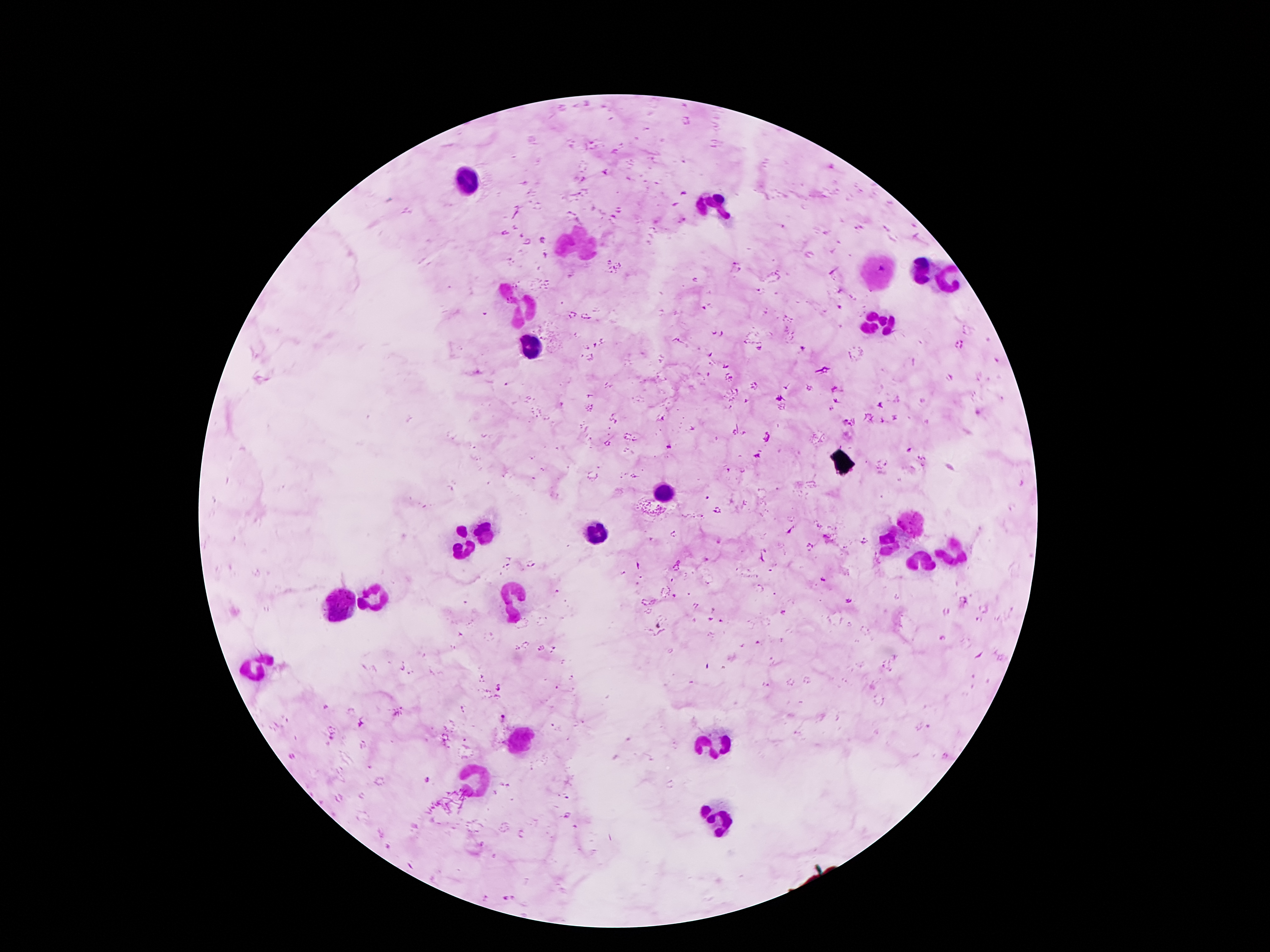

Approximate object centers, in pixels from the top-left corner.
Summary:
  - Plasmodium parasite locations: (x=736, y=260), (x=845, y=421), (x=850, y=425), (x=669, y=447), (x=707, y=497), (x=823, y=580), (x=504, y=717), (x=428, y=780), (x=567, y=815)
  - Leukocyte locations: (x=463, y=179), (x=714, y=208), (x=580, y=247), (x=921, y=270), (x=878, y=272), (x=949, y=277), (x=521, y=304), (x=880, y=324), (x=533, y=349), (x=662, y=490), (x=912, y=526), (x=485, y=529), (x=597, y=533), (x=891, y=542), (x=460, y=545), (x=953, y=554), (x=919, y=561), (x=372, y=597), (x=515, y=599), (x=340, y=606), (x=256, y=669), (x=521, y=736), (x=717, y=738), (x=480, y=779), (x=721, y=820)
  - Field of view: single
  - Magnification: 100x
  - Preparation: thick blood smear
  - Image size: 1270×952 pixels
  - Capture: smartphone camera through the microscope eyepiece
  - Stain: Giemsa
  - Patient malaria status: infected with Plasmodium falciparum